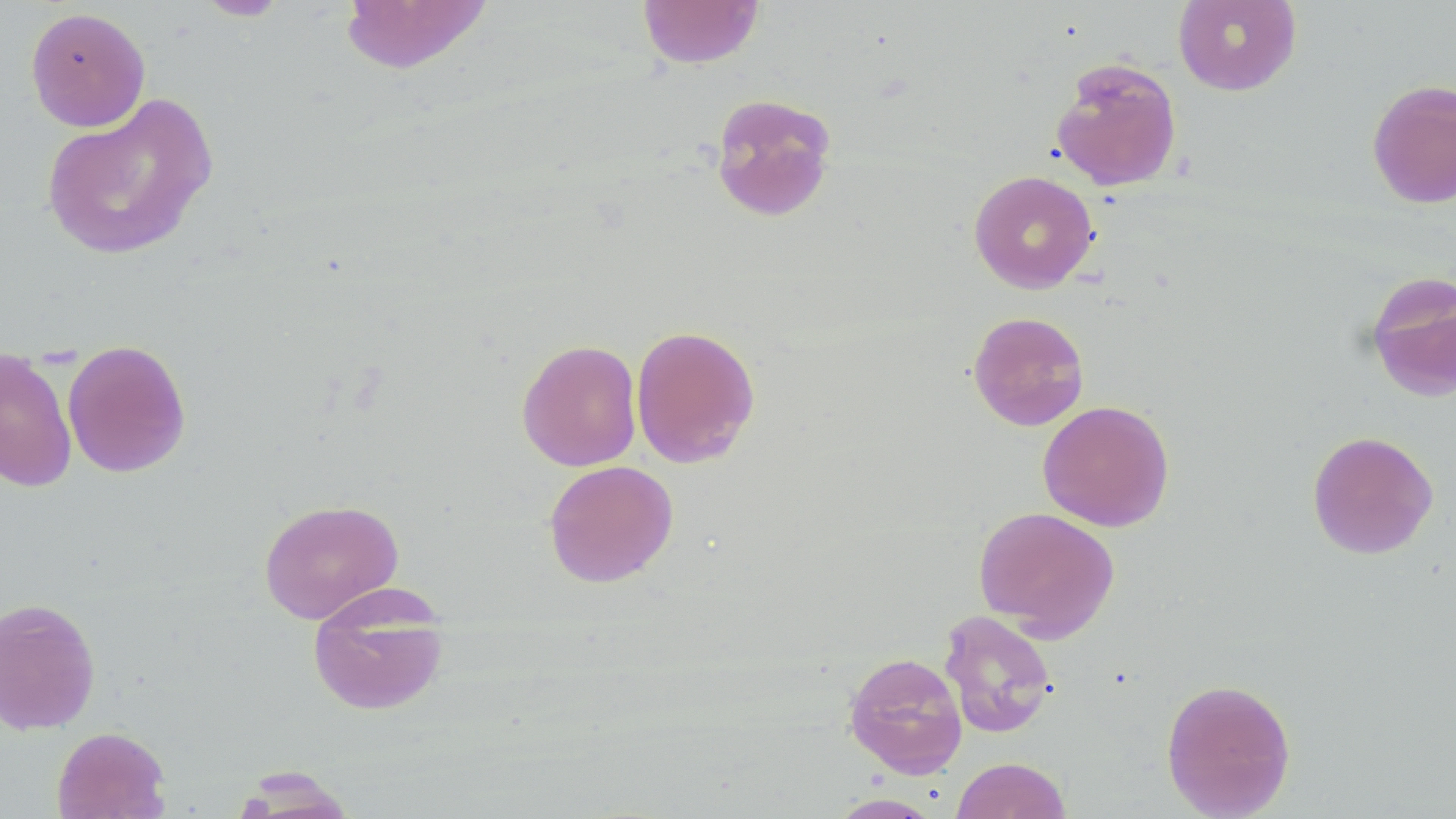
Approximate bounding boxes as named x1/y1/x2/y2 corners in pixels. Uninfected red blood cell locations: (x1=193, y1=0, x2=292, y2=21), (x1=637, y1=0, x2=764, y2=69), (x1=1173, y1=0, x2=1302, y2=96), (x1=339, y1=1, x2=494, y2=75), (x1=25, y1=6, x2=150, y2=132), (x1=1050, y1=57, x2=1183, y2=192), (x1=1366, y1=78, x2=1456, y2=209), (x1=40, y1=91, x2=219, y2=262), (x1=709, y1=92, x2=838, y2=222), (x1=968, y1=170, x2=1099, y2=293), (x1=1365, y1=271, x2=1456, y2=402), (x1=967, y1=311, x2=1090, y2=431), (x1=630, y1=323, x2=761, y2=468), (x1=516, y1=338, x2=642, y2=472), (x1=61, y1=339, x2=192, y2=478), (x1=0, y1=346, x2=77, y2=493), (x1=1037, y1=400, x2=1175, y2=532), (x1=1306, y1=429, x2=1438, y2=560), (x1=543, y1=459, x2=679, y2=588), (x1=258, y1=498, x2=404, y2=624), (x1=973, y1=506, x2=1120, y2=640), (x1=307, y1=592, x2=450, y2=717), (x1=0, y1=597, x2=102, y2=736), (x1=939, y1=609, x2=1057, y2=738), (x1=843, y1=651, x2=968, y2=778), (x1=1160, y1=677, x2=1296, y2=819), (x1=52, y1=726, x2=171, y2=818), (x1=951, y1=757, x2=1071, y2=819), (x1=235, y1=770, x2=360, y2=817), (x1=829, y1=794, x2=942, y2=818). Slide-level diagnosis: no evidence of blood parasites. Image is 1456×819 pixels. 1000x magnification. Single field of view. May-Grünwald-Giemsa stain. Light microscopy. Thin blood smear.